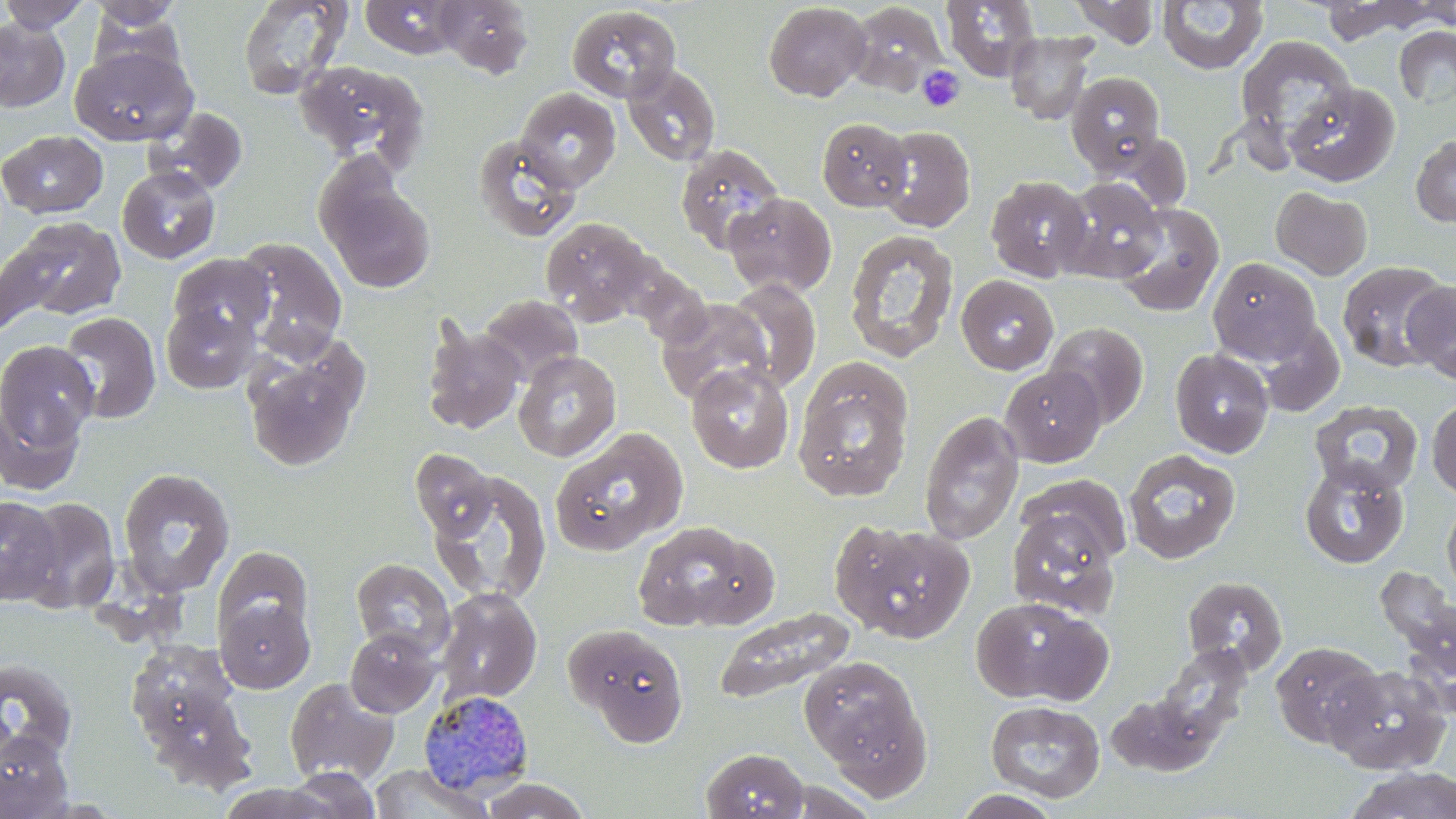
Approximate bounding boxes as (x1, y1, x2, y2) in pixels. Uninfected red blood cell locations: (0, 0, 91, 32), (360, 0, 464, 59), (435, 0, 533, 79), (942, 0, 1042, 82), (1319, 0, 1435, 44), (1414, 0, 1456, 29), (86, 1, 183, 30), (238, 1, 353, 100), (1068, 1, 1162, 48), (1157, 1, 1268, 76), (763, 2, 870, 101), (847, 2, 950, 95), (565, 5, 680, 103), (87, 7, 187, 82), (0, 17, 70, 112), (1393, 26, 1456, 108), (1006, 31, 1097, 124), (1235, 35, 1358, 150), (71, 46, 198, 145), (294, 60, 428, 168), (622, 63, 721, 166), (1067, 71, 1165, 176), (1284, 82, 1401, 187), (515, 88, 621, 192), (146, 107, 248, 195), (817, 117, 913, 211), (875, 125, 975, 232), (0, 129, 108, 218), (474, 132, 581, 241), (1411, 134, 1456, 228), (675, 143, 785, 255), (117, 166, 221, 264), (985, 176, 1092, 281), (322, 177, 435, 293), (1057, 177, 1167, 282), (1271, 186, 1373, 280), (724, 192, 837, 296), (1113, 202, 1225, 317), (7, 216, 126, 322), (539, 216, 660, 326), (843, 229, 959, 362), (235, 236, 348, 359), (168, 253, 274, 342), (1208, 257, 1322, 364), (1337, 260, 1451, 371), (956, 275, 1059, 375), (723, 279, 822, 392), (1401, 280, 1456, 383), (679, 283, 814, 452), (478, 295, 582, 387), (656, 298, 774, 404), (161, 304, 258, 394), (59, 311, 161, 424), (421, 319, 526, 435), (1045, 321, 1149, 429), (1254, 321, 1346, 417), (0, 339, 100, 473), (242, 341, 365, 471), (1170, 348, 1274, 458), (513, 350, 621, 462), (686, 363, 795, 474), (1000, 365, 1106, 466), (793, 370, 913, 502), (1427, 396, 1456, 501), (1310, 400, 1423, 495), (919, 410, 1025, 545), (550, 429, 686, 556), (409, 448, 496, 540), (1122, 449, 1241, 565), (1299, 459, 1410, 569), (117, 467, 236, 598), (429, 471, 552, 606), (1017, 474, 1133, 568), (0, 496, 62, 605), (18, 497, 120, 613), (1442, 497, 1456, 605), (1006, 507, 1123, 618), (829, 517, 975, 642), (630, 521, 767, 632), (213, 546, 313, 640), (79, 549, 194, 645), (351, 558, 456, 660), (1382, 566, 1455, 688), (1182, 576, 1288, 675), (436, 588, 542, 704), (971, 595, 1113, 706), (216, 597, 315, 693), (713, 608, 856, 706), (567, 624, 691, 746), (345, 627, 441, 717), (1271, 642, 1384, 748), (141, 644, 257, 797), (1154, 645, 1252, 752), (799, 655, 928, 783), (0, 658, 79, 764), (1327, 665, 1452, 775), (285, 677, 399, 784), (1106, 692, 1218, 777), (985, 700, 1106, 802), (0, 731, 73, 818), (700, 747, 809, 819), (367, 764, 496, 819), (1341, 766, 1456, 819), (282, 767, 381, 819), (476, 778, 593, 819), (215, 783, 343, 818), (952, 790, 1065, 819). Plasmodium malariae-infected red blood cell locations: (419, 690, 535, 797). Platelet locations: (918, 65, 964, 112). Slide-level diagnosis: Plasmodium malariae. Light microscopy. May-Grünwald-Giemsa stain. Thin blood smear. Single field of view. 1000x magnification. Image is 1456×819 pixels.